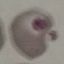

Malaria status: uninfected. Automatically extracted cell patch, resized to 64 × 64 pixels. Photographed with a smartphone camera at the microscope eyepiece. Giemsa-stained preparation. Thin smear of blood.